Outline each Plasmodium ovale-infected red blood cell.
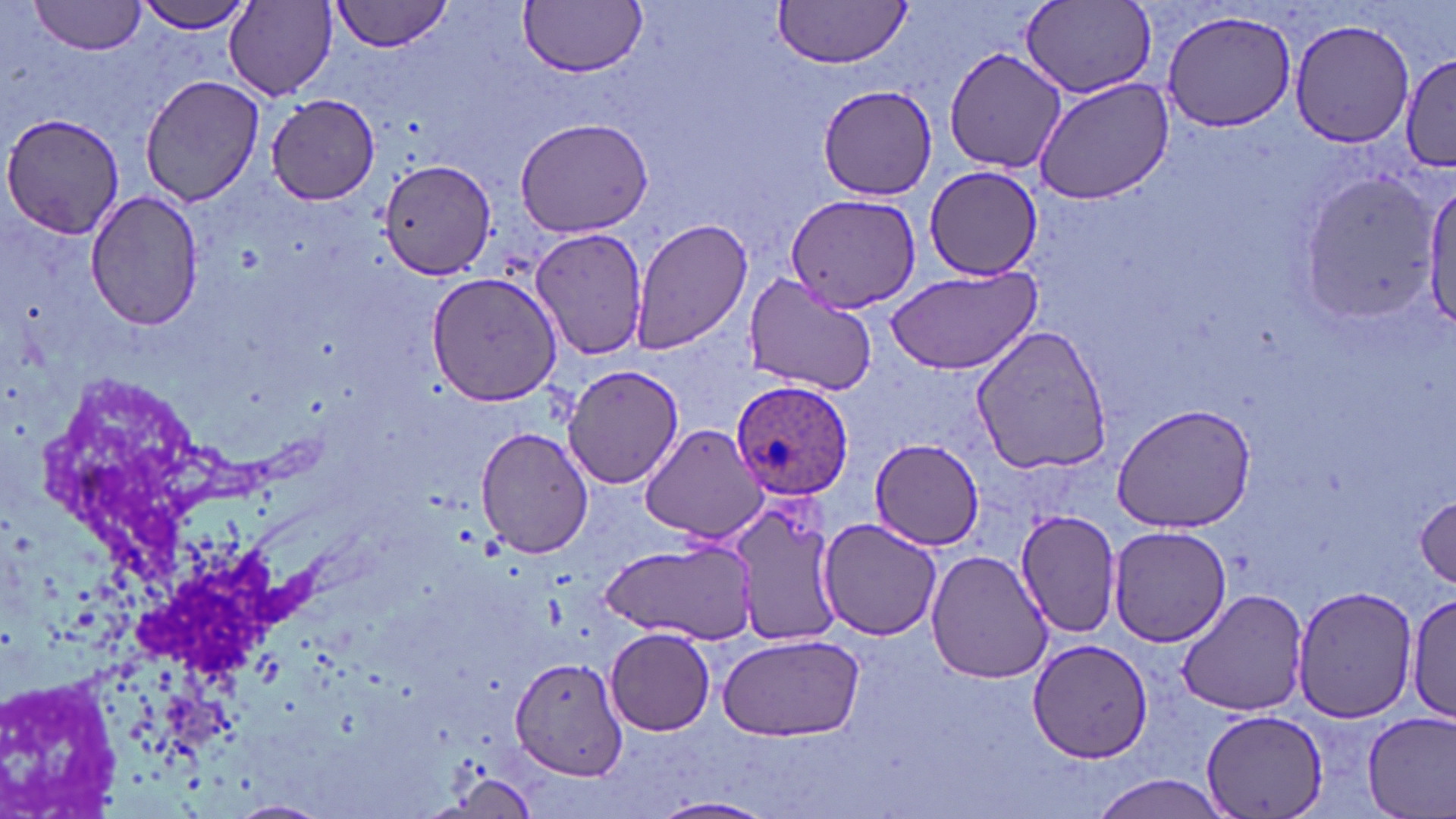

Approximate bounding boxes as named x1/y1/x2/y2 corners in pixels.
Plasmodium ovale-infected red blood cells: (x1=728, y1=380, x2=854, y2=500).

slide-level diagnosis = Plasmodium ovale
uninfected red blood cell locations = approximate bounding boxes as named x1/y1/x2/y2 corners in pixels: (x1=28, y1=0, x2=148, y2=54), (x1=136, y1=0, x2=255, y2=35), (x1=331, y1=0, x2=452, y2=52), (x1=518, y1=1, x2=646, y2=77), (x1=772, y1=1, x2=912, y2=68), (x1=225, y1=3, x2=337, y2=99), (x1=1022, y1=3, x2=1157, y2=101), (x1=1160, y1=7, x2=1297, y2=133), (x1=1289, y1=17, x2=1416, y2=149), (x1=943, y1=45, x2=1069, y2=175), (x1=1402, y1=50, x2=1453, y2=177), (x1=139, y1=74, x2=264, y2=208), (x1=1033, y1=75, x2=1174, y2=206), (x1=818, y1=83, x2=938, y2=200), (x1=265, y1=94, x2=380, y2=204), (x1=2, y1=112, x2=127, y2=241), (x1=513, y1=116, x2=655, y2=238), (x1=378, y1=157, x2=494, y2=283), (x1=924, y1=166, x2=1044, y2=278), (x1=1298, y1=170, x2=1441, y2=324), (x1=1424, y1=175, x2=1456, y2=331), (x1=86, y1=190, x2=205, y2=330), (x1=784, y1=192, x2=921, y2=316), (x1=631, y1=217, x2=753, y2=357), (x1=531, y1=229, x2=649, y2=361), (x1=885, y1=267, x2=1041, y2=376), (x1=426, y1=271, x2=562, y2=408), (x1=741, y1=276, x2=878, y2=396), (x1=970, y1=323, x2=1114, y2=476), (x1=562, y1=362, x2=683, y2=488), (x1=1111, y1=403, x2=1257, y2=533), (x1=637, y1=423, x2=770, y2=544), (x1=476, y1=426, x2=593, y2=559), (x1=869, y1=439, x2=984, y2=548), (x1=1413, y1=492, x2=1455, y2=589), (x1=732, y1=502, x2=840, y2=646), (x1=1016, y1=508, x2=1123, y2=639), (x1=816, y1=518, x2=943, y2=641), (x1=1109, y1=526, x2=1232, y2=646), (x1=601, y1=539, x2=758, y2=643), (x1=925, y1=550, x2=1055, y2=684), (x1=1292, y1=585, x2=1417, y2=724), (x1=1176, y1=588, x2=1312, y2=716), (x1=1408, y1=593, x2=1454, y2=721), (x1=607, y1=629, x2=715, y2=735), (x1=719, y1=633, x2=865, y2=743), (x1=1026, y1=641, x2=1152, y2=766), (x1=511, y1=658, x2=627, y2=783), (x1=0, y1=674, x2=126, y2=815), (x1=1201, y1=709, x2=1329, y2=819), (x1=1360, y1=710, x2=1456, y2=818), (x1=438, y1=766, x2=540, y2=817), (x1=1085, y1=775, x2=1232, y2=818), (x1=652, y1=797, x2=775, y2=818), (x1=229, y1=799, x2=330, y2=818)
preparation = thin blood smear
image size = 1456×819 pixels
stain = May-Grünwald-Giemsa
magnification = 1000x
field of view = one of a larger specimen
modality = light microscopy